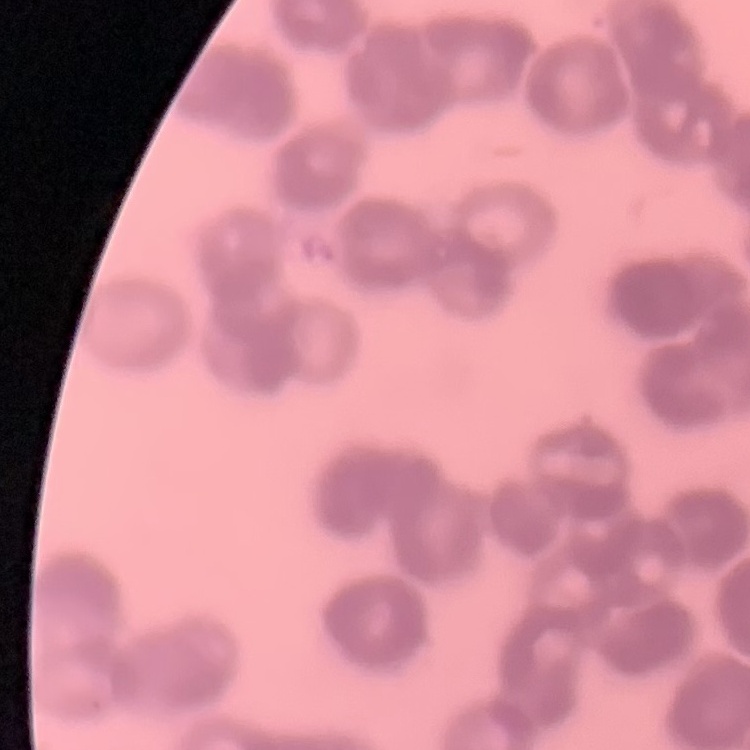

Summary:
  - Red blood cell morphology: rouleaux formation
  - Stain: Field's or Giemsa
  - Preparation: thin peripheral smear
  - Image type: one tile cut from a larger photomicrograph